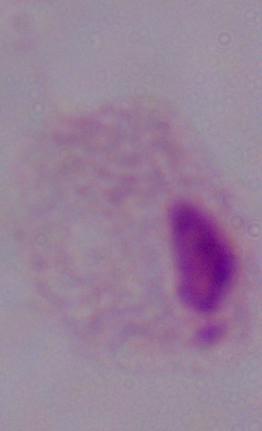

A trichomonad is shown. Micrograph. Captured at 1000x magnification.